Name the blood parasite species.
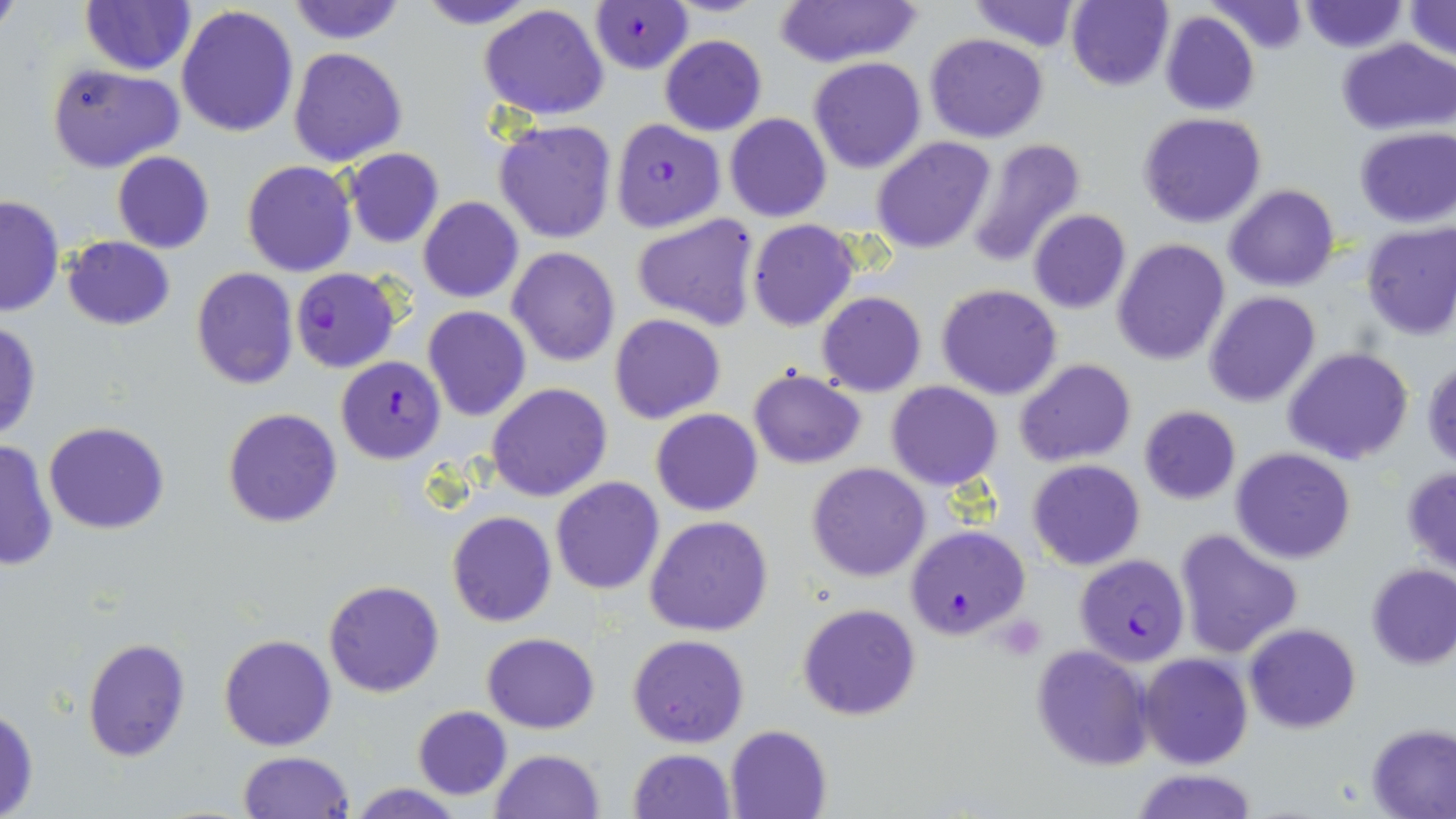
Plasmodium falciparum.

Approximate bounding boxes as named x1/y1/x2/y2 corners in pixels. Plasmodium falciparum-infected red blood cell locations: (x1=588, y1=2, x2=692, y2=73), (x1=609, y1=119, x2=725, y2=233), (x1=291, y1=268, x2=400, y2=373), (x1=335, y1=357, x2=446, y2=464), (x1=908, y1=525, x2=1028, y2=639), (x1=1073, y1=554, x2=1190, y2=666). Platelet locations: (x1=997, y1=614, x2=1048, y2=657). Uninfected red blood cell locations: (x1=0, y1=0, x2=22, y2=40), (x1=285, y1=0, x2=407, y2=44), (x1=412, y1=0, x2=544, y2=29), (x1=776, y1=0, x2=918, y2=68), (x1=965, y1=0, x2=1085, y2=53), (x1=79, y1=1, x2=195, y2=75), (x1=1067, y1=1, x2=1175, y2=91), (x1=1204, y1=1, x2=1309, y2=55), (x1=1298, y1=1, x2=1407, y2=52), (x1=1401, y1=1, x2=1455, y2=62), (x1=478, y1=3, x2=610, y2=121), (x1=176, y1=4, x2=301, y2=139), (x1=1159, y1=10, x2=1258, y2=116), (x1=924, y1=32, x2=1049, y2=143), (x1=659, y1=35, x2=766, y2=134), (x1=1339, y1=37, x2=1454, y2=135), (x1=289, y1=46, x2=409, y2=166), (x1=809, y1=56, x2=926, y2=173), (x1=47, y1=62, x2=184, y2=173), (x1=1138, y1=112, x2=1267, y2=228), (x1=725, y1=113, x2=831, y2=222), (x1=492, y1=118, x2=619, y2=244), (x1=1354, y1=126, x2=1455, y2=229), (x1=870, y1=136, x2=997, y2=254), (x1=962, y1=137, x2=1088, y2=268), (x1=343, y1=148, x2=445, y2=248), (x1=111, y1=151, x2=215, y2=254), (x1=241, y1=160, x2=356, y2=277), (x1=1223, y1=183, x2=1340, y2=291), (x1=0, y1=196, x2=64, y2=316), (x1=418, y1=197, x2=524, y2=303), (x1=1027, y1=209, x2=1130, y2=314), (x1=631, y1=214, x2=762, y2=332), (x1=747, y1=220, x2=859, y2=333), (x1=1360, y1=221, x2=1456, y2=340), (x1=62, y1=236, x2=175, y2=331), (x1=1112, y1=239, x2=1230, y2=366), (x1=506, y1=246, x2=621, y2=365), (x1=191, y1=267, x2=299, y2=389), (x1=937, y1=283, x2=1063, y2=400), (x1=817, y1=291, x2=927, y2=395), (x1=1204, y1=291, x2=1321, y2=406), (x1=423, y1=306, x2=531, y2=422), (x1=609, y1=314, x2=724, y2=423), (x1=0, y1=321, x2=42, y2=441), (x1=1283, y1=347, x2=1414, y2=465), (x1=1013, y1=358, x2=1136, y2=467), (x1=1423, y1=358, x2=1456, y2=470), (x1=748, y1=367, x2=866, y2=469), (x1=885, y1=381, x2=1003, y2=491), (x1=487, y1=383, x2=612, y2=502), (x1=1137, y1=405, x2=1241, y2=504), (x1=223, y1=408, x2=343, y2=528), (x1=651, y1=409, x2=763, y2=516), (x1=43, y1=422, x2=170, y2=534), (x1=0, y1=437, x2=58, y2=573), (x1=1232, y1=447, x2=1355, y2=564), (x1=1028, y1=459, x2=1145, y2=570), (x1=807, y1=463, x2=931, y2=582), (x1=1401, y1=468, x2=1456, y2=574), (x1=551, y1=476, x2=665, y2=594), (x1=446, y1=511, x2=558, y2=628), (x1=645, y1=516, x2=774, y2=638), (x1=1175, y1=528, x2=1304, y2=657), (x1=1366, y1=562, x2=1456, y2=668), (x1=323, y1=579, x2=446, y2=698), (x1=797, y1=602, x2=921, y2=721), (x1=1244, y1=623, x2=1362, y2=733), (x1=482, y1=632, x2=600, y2=734), (x1=218, y1=633, x2=338, y2=751), (x1=627, y1=634, x2=749, y2=748), (x1=81, y1=636, x2=191, y2=763), (x1=1030, y1=646, x2=1152, y2=772), (x1=1139, y1=653, x2=1253, y2=770), (x1=411, y1=704, x2=511, y2=799), (x1=0, y1=706, x2=39, y2=819), (x1=1366, y1=723, x2=1455, y2=817), (x1=725, y1=725, x2=832, y2=818), (x1=628, y1=748, x2=736, y2=819), (x1=490, y1=749, x2=605, y2=819), (x1=237, y1=750, x2=357, y2=818), (x1=1130, y1=768, x2=1257, y2=819), (x1=349, y1=782, x2=465, y2=819). Thin blood smear. Image is 1456×819 pixels. Single field of view. 1000x magnification. May-Grünwald-Giemsa stain. Light microscopy.